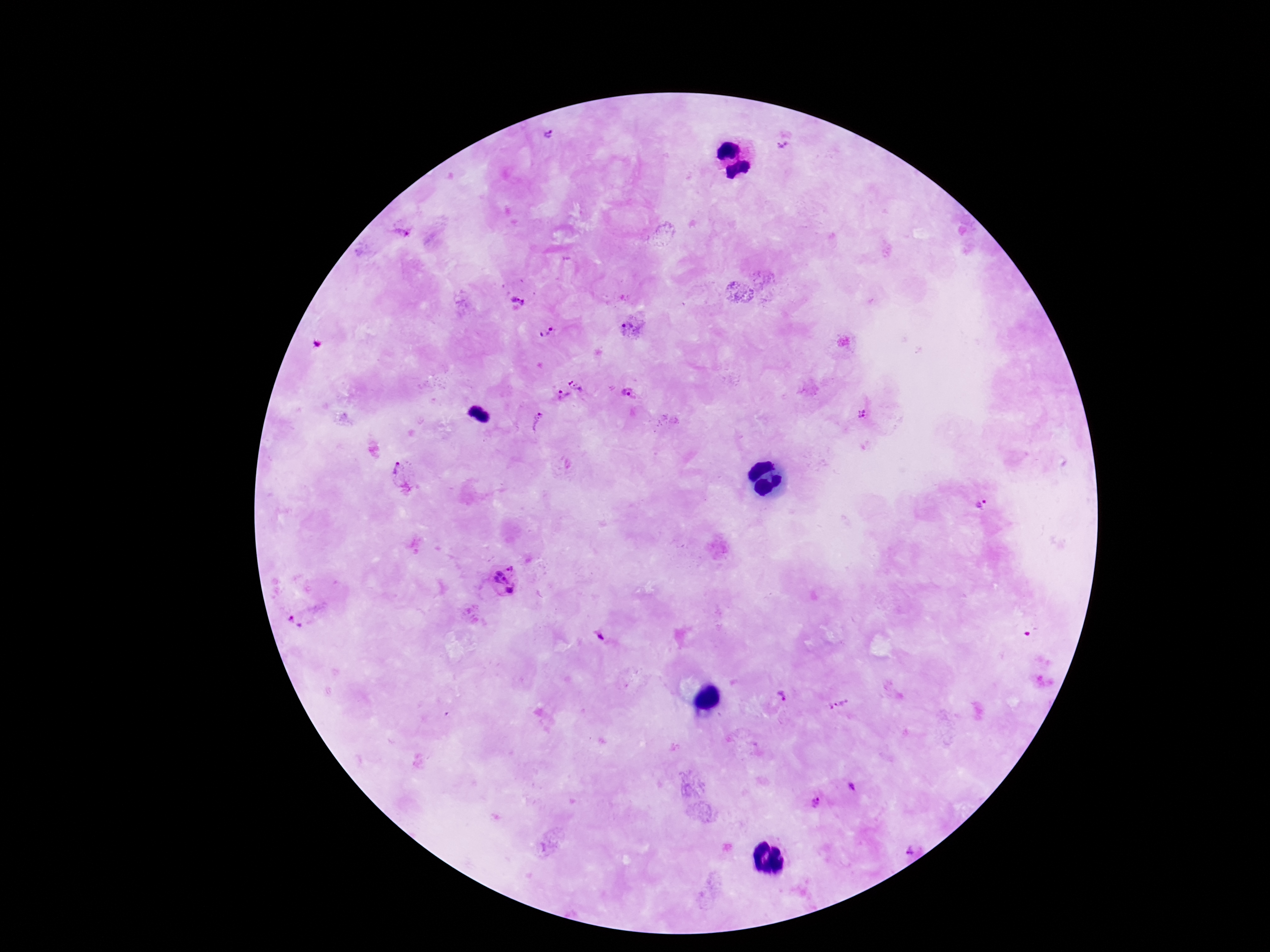

Approximate object centers, in pixels from the top-left corner. Plasmodium parasite locations: (x=555, y=136), (x=781, y=146), (x=401, y=234), (x=517, y=301), (x=635, y=326), (x=547, y=333), (x=578, y=381), (x=632, y=394), (x=561, y=397), (x=862, y=415), (x=539, y=422), (x=401, y=473), (x=983, y=502), (x=504, y=580), (x=301, y=619), (x=599, y=636), (x=780, y=694), (x=838, y=704), (x=855, y=780), (x=813, y=798), (x=907, y=841). Thick blood smear. Smartphone photograph taken through the microscope eyepiece. Image is 1270×952 pixels. Patient malaria status: positive. 100x magnification. One field from this slide. Giemsa-stained preparation.